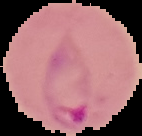

Summary:
  - Image size: 142×136 pixels
  - Preparation: thin blood smear
  - Image type: cell region segmented out of the field of view; surrounding area masked to black
  - Malaria status: parasitized